Locate every Plasmodium parasite.
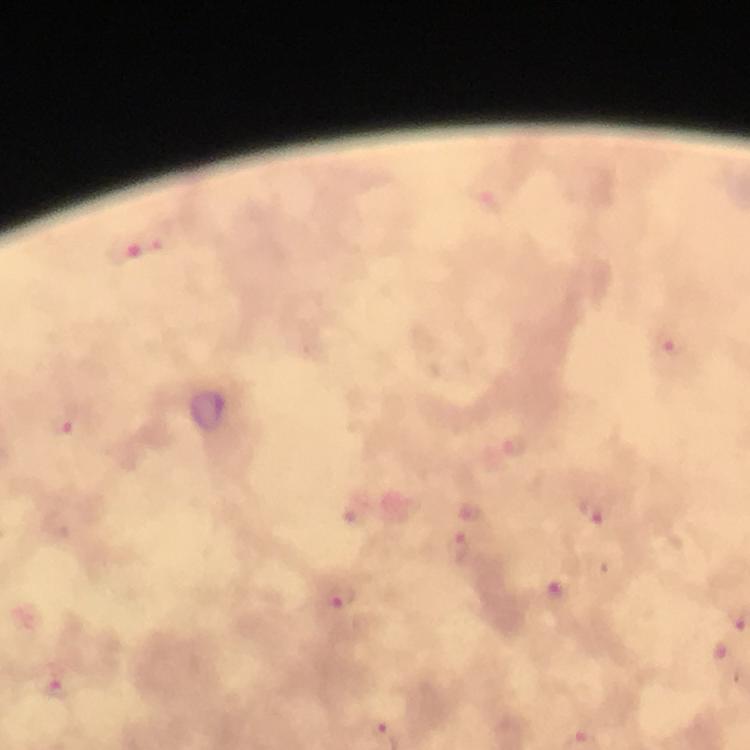

Approximate centers as [x, y] in pixels.
Plasmodium parasites: [137, 251], [674, 344], [68, 426], [516, 445], [593, 514], [458, 548], [558, 593], [339, 596], [725, 653], [56, 689].

Immersion oil applied. Thick blood smear. Photographed through the microscope with a smartphone camera. Cropped region of a single field of view. From a diagnostic examination for malaria. At 100x magnification. Giemsa stain. Image is 750×750 pixels.